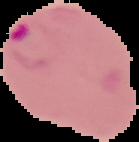
image_size: 139×142 pixels
preparation: thin blood smear
result: malaria parasites identified
image_type: segmented cell region with the area outside set to black